Classify this cell by malaria status.
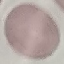

It is uninfected.

Summary:
  - Capture: smartphone camera at the microscope eyepiece
  - Stain: Giemsa
  - Image type: automatically extracted cell patch, resized to 64 × 64 pixels
  - Preparation: thin blood film